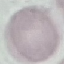
Summary:
  - Result: no malaria parasites seen
  - Preparation: thin blood smear
  - Image type: automatically extracted cell patch, resized to 64 × 64 pixels
  - Stain: Giemsa
  - Capture: smartphone camera at the microscope eyepiece